Evaluate for malaria.
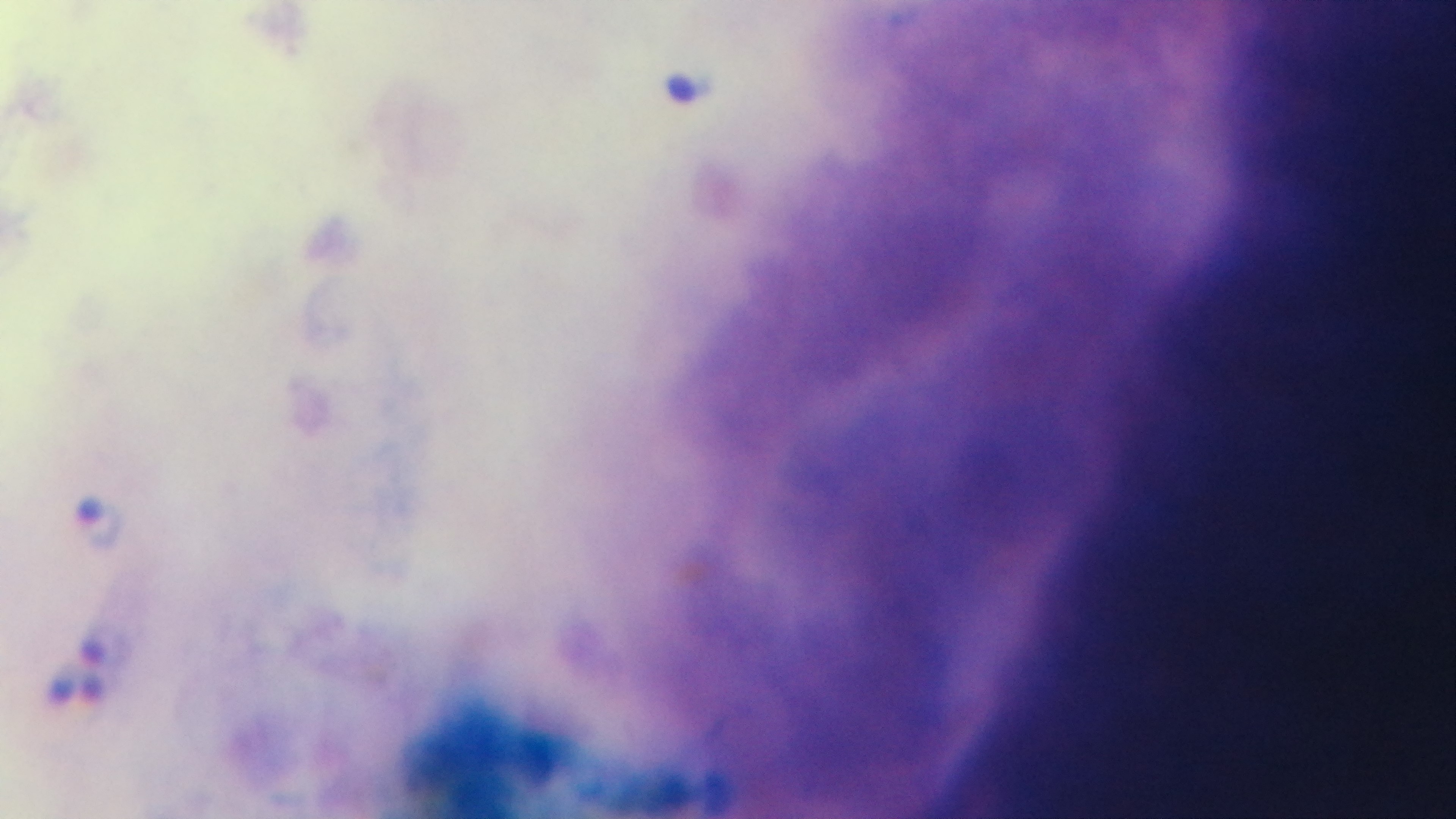
Infected.

{
  "field_of_view": "one from the slide",
  "modality": "light microscopy",
  "preparation": "thick blood film",
  "capture": "mounted 4K digital camera",
  "stain": "Giemsa",
  "objective": "100x oil immersion"
}